Give the extent of all Plasmodium falciparum-infected red blood cells.
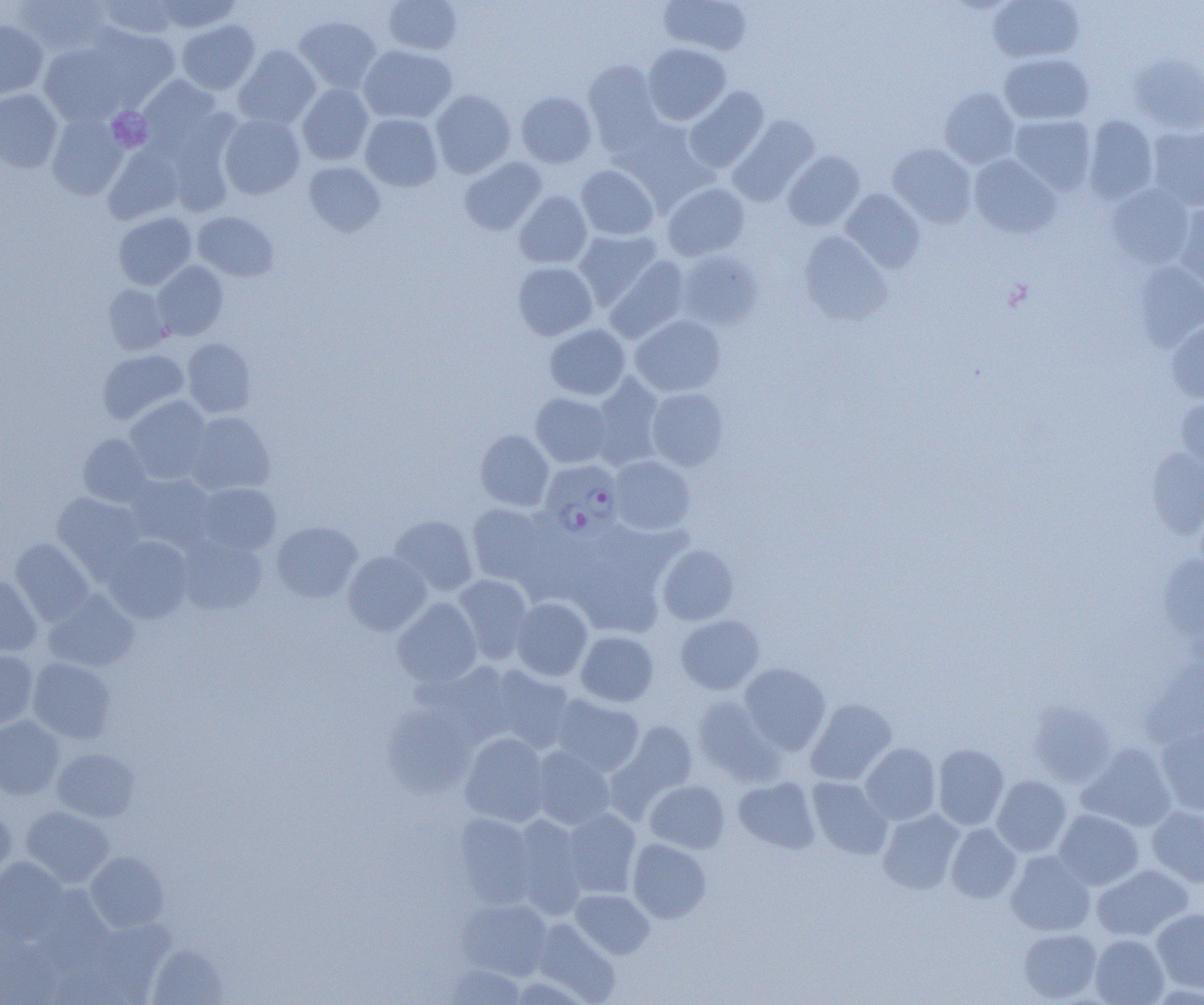
Approximate bounding boxes as [x1, y1, x2, y2] in pixels.
Plasmodium falciparum-infected red blood cells: [540, 460, 624, 538].

{
  "slide_level_diagnosis": "Plasmodium falciparum",
  "modality": "optical microscopy",
  "platelet_locations": "approximate bounding boxes as [x1, y1, x2, y2] in pixels: [106, 106, 153, 152]",
  "field_of_view": "single",
  "magnification": "1000x",
  "uninfected_red_blood_cell_locations": "approximate bounding boxes as [x1, y1, x2, y2] in pixels: [14, 0, 112, 56], [94, 0, 179, 40], [153, 0, 242, 33], [383, 0, 462, 55], [658, 0, 752, 56], [987, 0, 1085, 63], [294, 15, 382, 92], [0, 20, 49, 99], [176, 20, 260, 95], [85, 26, 179, 108], [643, 42, 731, 125], [38, 43, 128, 125], [359, 44, 458, 123], [233, 45, 321, 129], [999, 53, 1094, 124], [1129, 54, 1204, 133], [583, 58, 664, 151], [137, 74, 223, 153], [297, 84, 374, 165], [684, 86, 769, 172], [939, 88, 1020, 168], [0, 89, 62, 172], [431, 89, 516, 178], [516, 91, 597, 168], [47, 113, 128, 200], [360, 113, 443, 191], [219, 114, 305, 199], [1009, 115, 1096, 195], [1082, 115, 1158, 204], [728, 116, 819, 206], [164, 121, 239, 218], [1147, 126, 1204, 211], [103, 143, 185, 224], [888, 143, 976, 227], [783, 150, 865, 231], [969, 154, 1061, 238], [458, 156, 546, 235], [304, 162, 385, 236], [576, 165, 659, 240], [663, 183, 749, 260], [1105, 183, 1195, 268], [1121, 184, 1200, 348], [841, 189, 925, 272], [514, 191, 592, 268], [1174, 204, 1204, 295], [192, 211, 278, 281], [113, 212, 197, 290], [573, 229, 662, 308], [798, 232, 893, 327], [677, 250, 762, 330], [605, 256, 690, 343], [153, 261, 228, 340], [513, 261, 598, 340], [1132, 262, 1204, 350], [102, 285, 172, 355], [630, 314, 727, 397], [1167, 319, 1204, 402], [544, 323, 631, 400], [183, 338, 257, 418], [97, 349, 189, 425], [589, 375, 664, 469], [647, 387, 729, 471], [530, 393, 614, 468], [1176, 395, 1204, 477], [124, 396, 213, 484], [184, 411, 275, 495], [475, 429, 555, 511], [77, 433, 151, 506], [1144, 448, 1204, 539], [608, 455, 695, 536], [126, 473, 217, 551], [196, 482, 281, 555], [52, 493, 146, 577], [467, 503, 557, 589], [388, 515, 480, 596], [271, 521, 363, 602], [565, 525, 682, 633], [103, 536, 194, 623], [176, 536, 267, 616], [11, 538, 95, 625], [657, 545, 739, 625], [342, 551, 432, 636], [1158, 555, 1204, 649], [0, 574, 42, 657], [453, 574, 534, 664], [44, 591, 140, 672], [510, 597, 593, 681], [392, 598, 483, 687], [675, 615, 764, 694], [575, 630, 659, 706], [0, 650, 39, 730], [1141, 655, 1203, 751], [27, 657, 116, 744], [414, 660, 516, 745], [739, 663, 831, 754], [483, 664, 575, 753], [550, 693, 645, 776], [693, 694, 783, 783], [805, 698, 897, 786], [1028, 701, 1117, 787], [383, 706, 476, 797], [0, 716, 65, 800], [612, 720, 699, 809], [1155, 728, 1204, 816], [459, 732, 550, 827], [860, 742, 941, 825], [933, 743, 1009, 830], [1077, 743, 1177, 832], [531, 746, 615, 830], [53, 747, 140, 822], [992, 775, 1072, 856], [733, 776, 820, 854], [807, 777, 891, 859], [644, 780, 730, 854], [0, 806, 16, 883], [20, 806, 114, 887], [1147, 806, 1204, 887], [560, 809, 641, 898], [878, 809, 965, 894], [1053, 809, 1144, 889], [454, 813, 538, 907], [510, 816, 588, 916], [946, 823, 1022, 903], [628, 838, 711, 923], [1005, 851, 1095, 936], [85, 852, 169, 932], [0, 858, 68, 940], [1091, 864, 1193, 942], [570, 889, 654, 959], [457, 898, 552, 980], [1152, 908, 1204, 993], [530, 918, 620, 1003], [1019, 928, 1102, 1002], [1090, 934, 1169, 1005], [0, 938, 62, 1004], [147, 944, 228, 1004], [443, 964, 526, 1004]",
  "image_size": "1204×1005 pixels",
  "preparation": "thin blood film"
}